Name the blood parasite species.
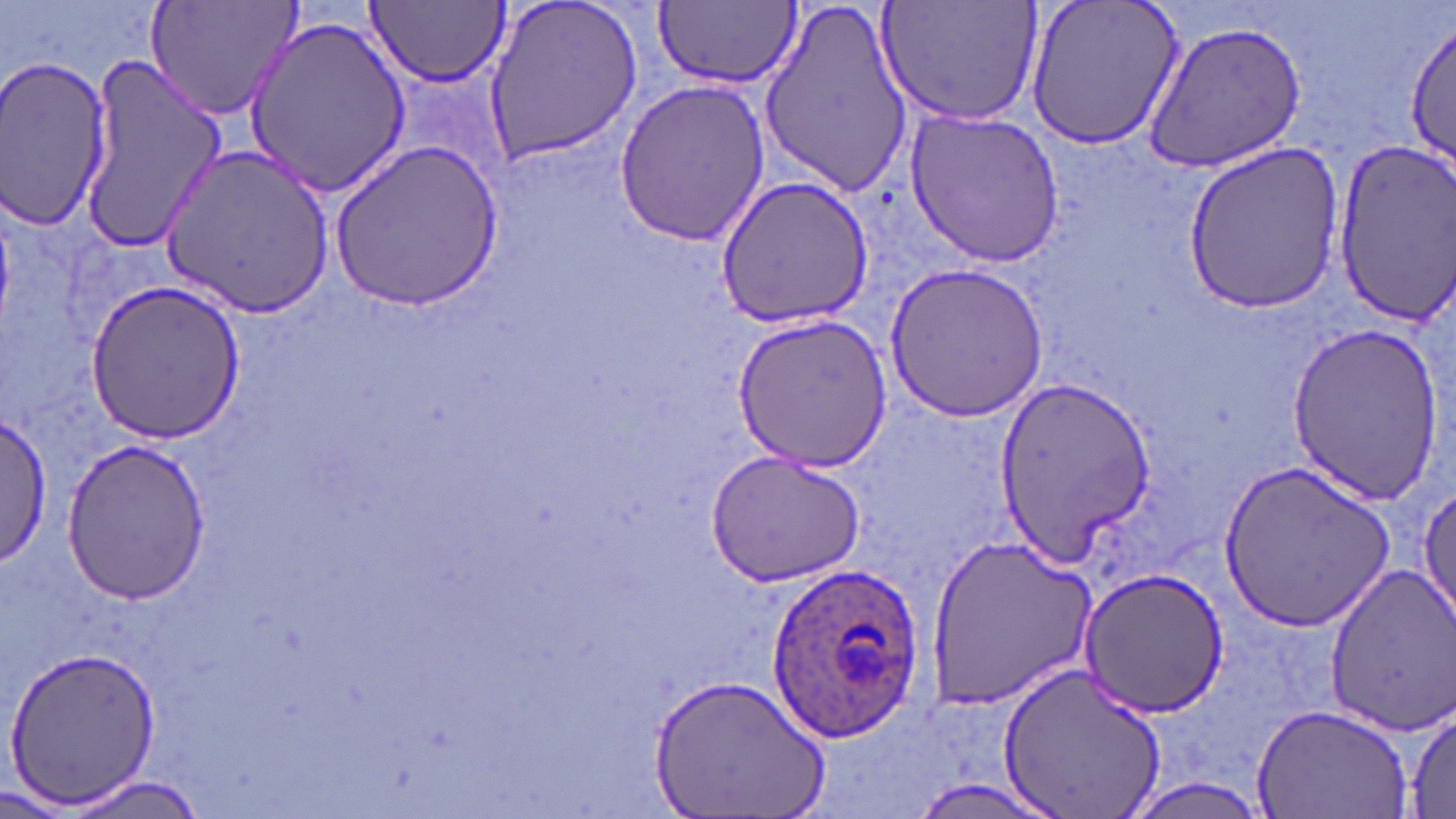

Plasmodium ovale.

Summary:
  - Coordinate format: approximate bounding boxes as (x1, y1, x2, y2) in pixels
  - Plasmodium ovale-infected red blood cell locations: (765, 558, 927, 741)
  - Uninfected red blood cell locations: (147, 0, 304, 121), (481, 0, 643, 165), (757, 0, 915, 198), (876, 0, 1044, 128), (1025, 0, 1186, 152), (364, 1, 510, 90), (651, 1, 802, 91), (243, 13, 411, 199), (1405, 18, 1455, 173), (1141, 20, 1308, 172), (77, 47, 225, 251), (0, 57, 116, 233), (614, 77, 771, 248), (905, 108, 1064, 265), (330, 140, 503, 311), (1177, 143, 1351, 315), (1331, 144, 1456, 321), (161, 145, 336, 317), (715, 175, 876, 329), (883, 262, 1048, 423), (85, 279, 246, 445), (734, 315, 892, 470), (1283, 319, 1444, 505), (995, 374, 1154, 566), (0, 414, 52, 568), (59, 441, 215, 605), (704, 451, 865, 587), (1218, 459, 1397, 631), (1413, 481, 1455, 629), (925, 534, 1100, 706), (1076, 564, 1229, 717), (1325, 565, 1456, 734), (5, 644, 162, 808), (995, 658, 1169, 819), (651, 673, 831, 819), (1405, 700, 1456, 818), (1252, 701, 1414, 818), (64, 772, 212, 818), (0, 782, 79, 817)
  - Image size: 1456×819 pixels
  - Magnification: 1000x
  - Preparation: thin blood smear
  - Field of view: one of a larger specimen
  - Modality: light microscopy
  - Stain: May-Grünwald-Giemsa